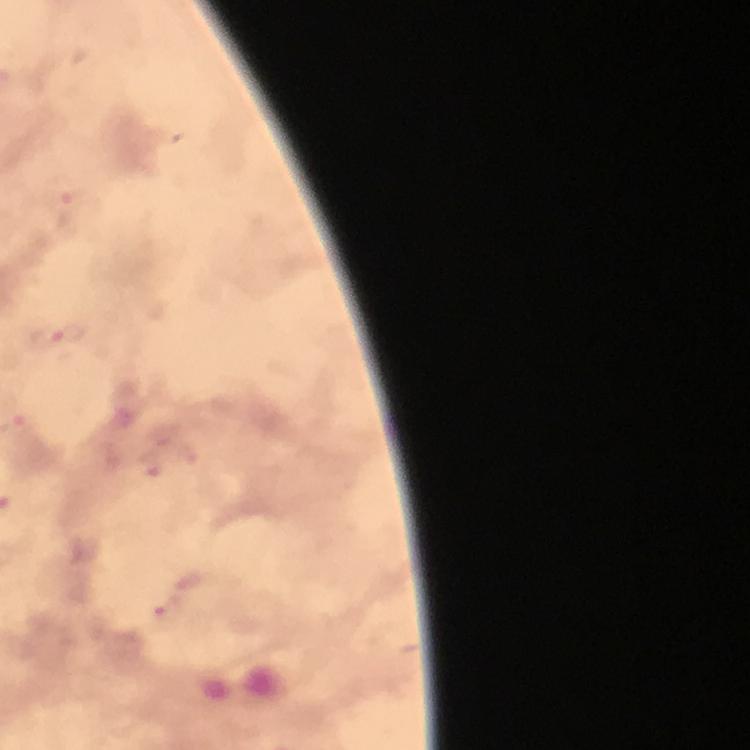

Approximate centers as [x, y] in pixels.
Summary:
  - Malaria parasite locations: [73, 209], [59, 337], [172, 614]
  - Magnification: 100x
  - Preparation: thick blood smear
  - Context: from a diagnostic examination for malaria
  - Image size: 750×750 pixels
  - Capture: smartphone photograph through a microscope
  - Stain: Giemsa
  - Cropped from: one field of view
  - Immersion oil: applied